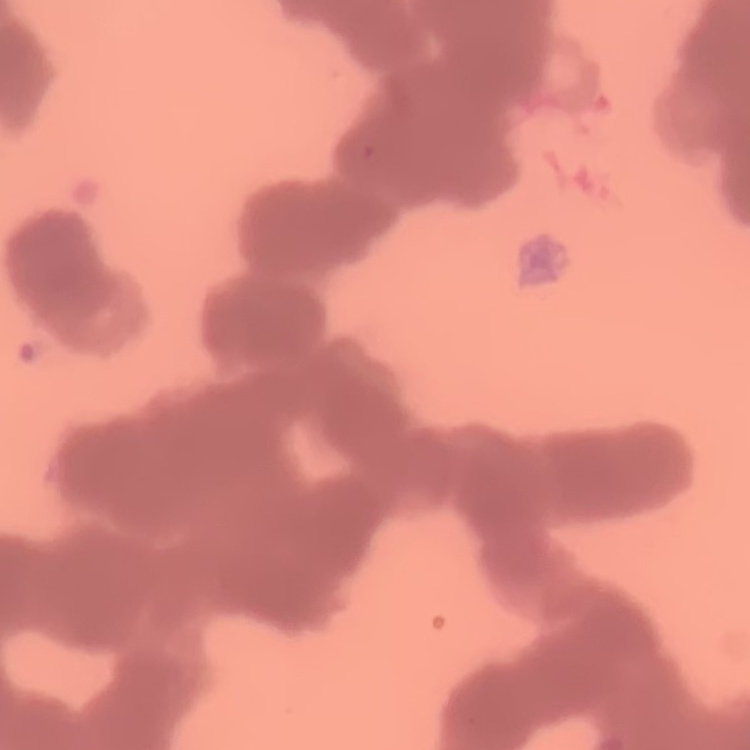

erythrocyte morphology = rouleaux formation
image type = square crop of a larger photomicrograph
stain = Field's or Giemsa
preparation = thin blood smear